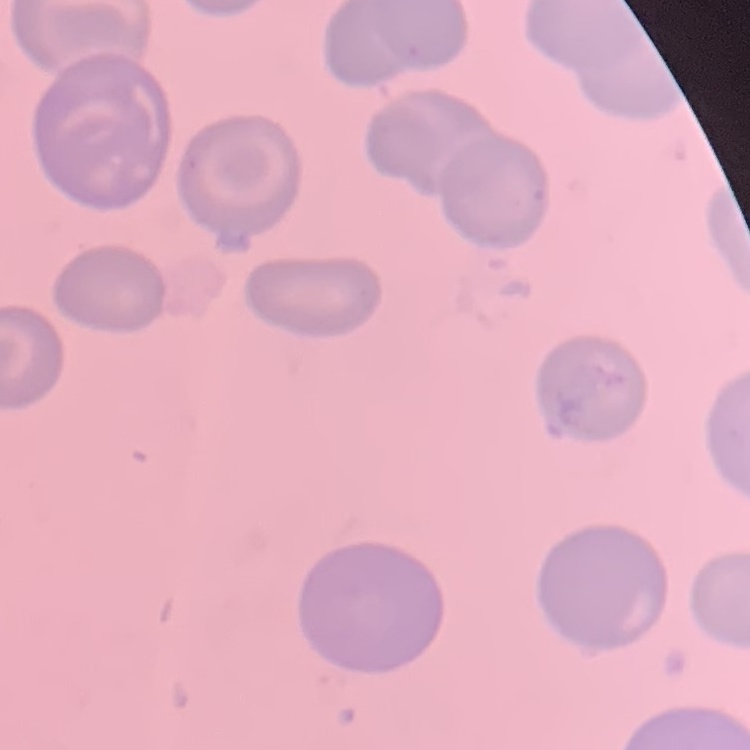
The erythrocytes show no rouleaux formation. Thin peripheral smear. Stained with either Field's or Giemsa. Square crop of a larger photomicrograph.